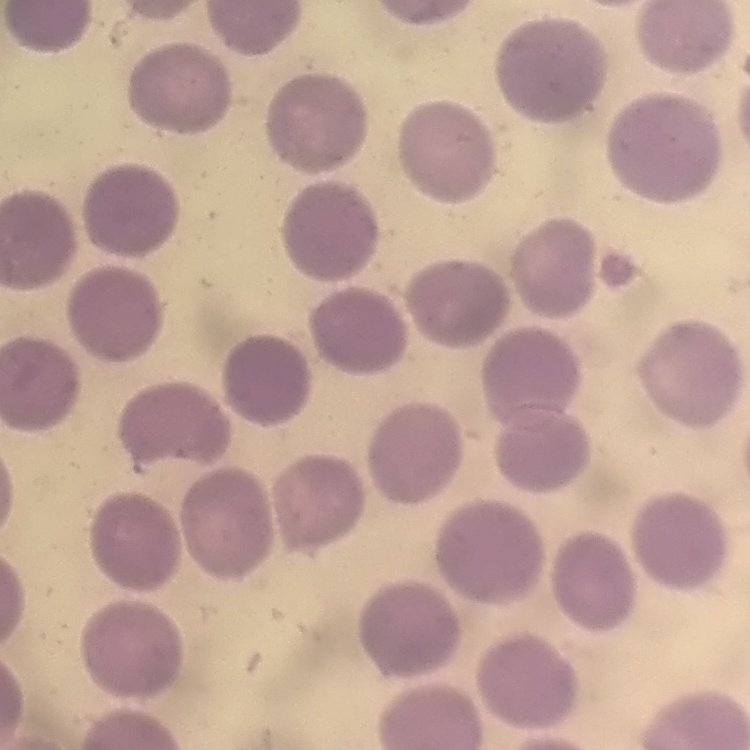
The erythrocytes exhibit no rouleaux formation. Square crop of a larger photomicrograph. Field's or Giemsa stain. Thin blood smear.